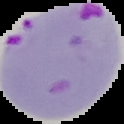 Segmented cell region on a black background. Result: malaria parasites identified. Image is 124×124 pixels. From a thin blood smear.